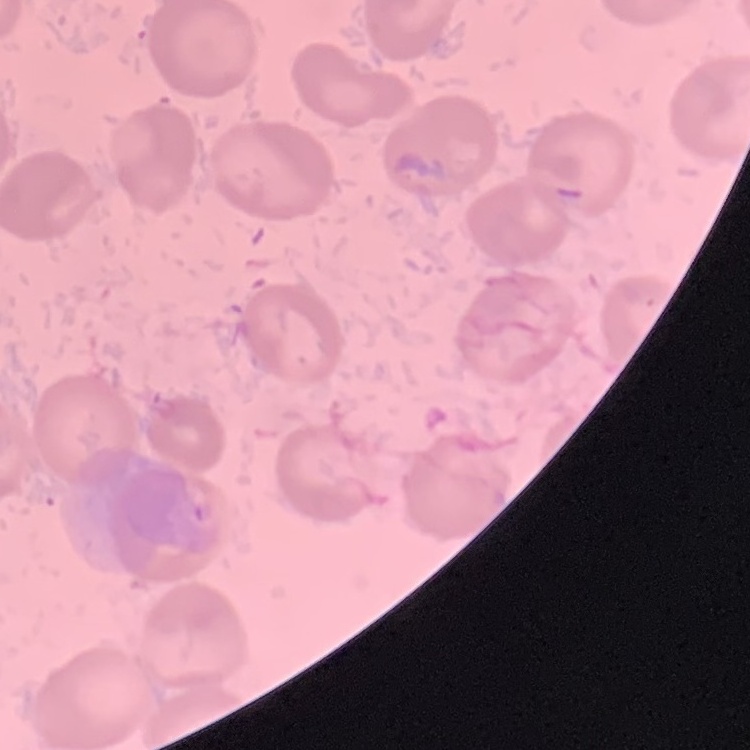
Summary:
  - Erythrocyte morphology: no rouleaux formation
  - Image type: one tile cut from a larger photomicrograph
  - Stain: Field's or Giemsa
  - Preparation: thin blood film